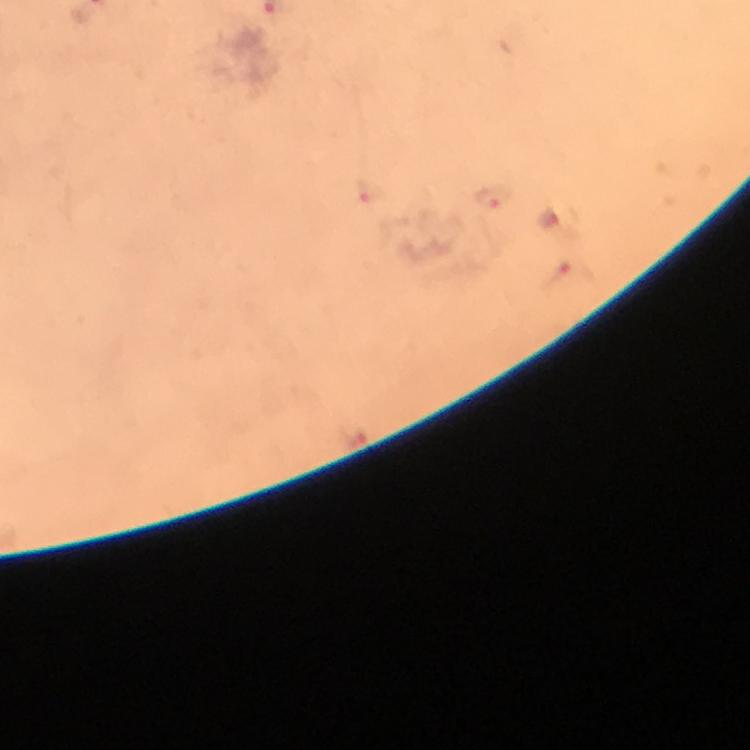

Approximate object centers, in pixels from the top-left corner.
Summary:
  - Plasmodium parasite locations: (x=492, y=198), (x=549, y=219), (x=574, y=273)
  - Context: from a malaria diagnostic workup
  - Magnification: 100x
  - Cropped from: one field of view
  - Immersion oil: used
  - Image size: 750×750 pixels
  - Stain: Giemsa
  - Capture: smartphone mounted on the microscope
  - Preparation: thick smear